Report the malaria status of this cell.
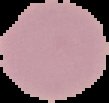

Uninfected.

From a thin blood smear. Image is 109×103 pixels. Cell region segmented out of the field of view; the surrounding area is masked to black.